Locate and identify every blood parasite.
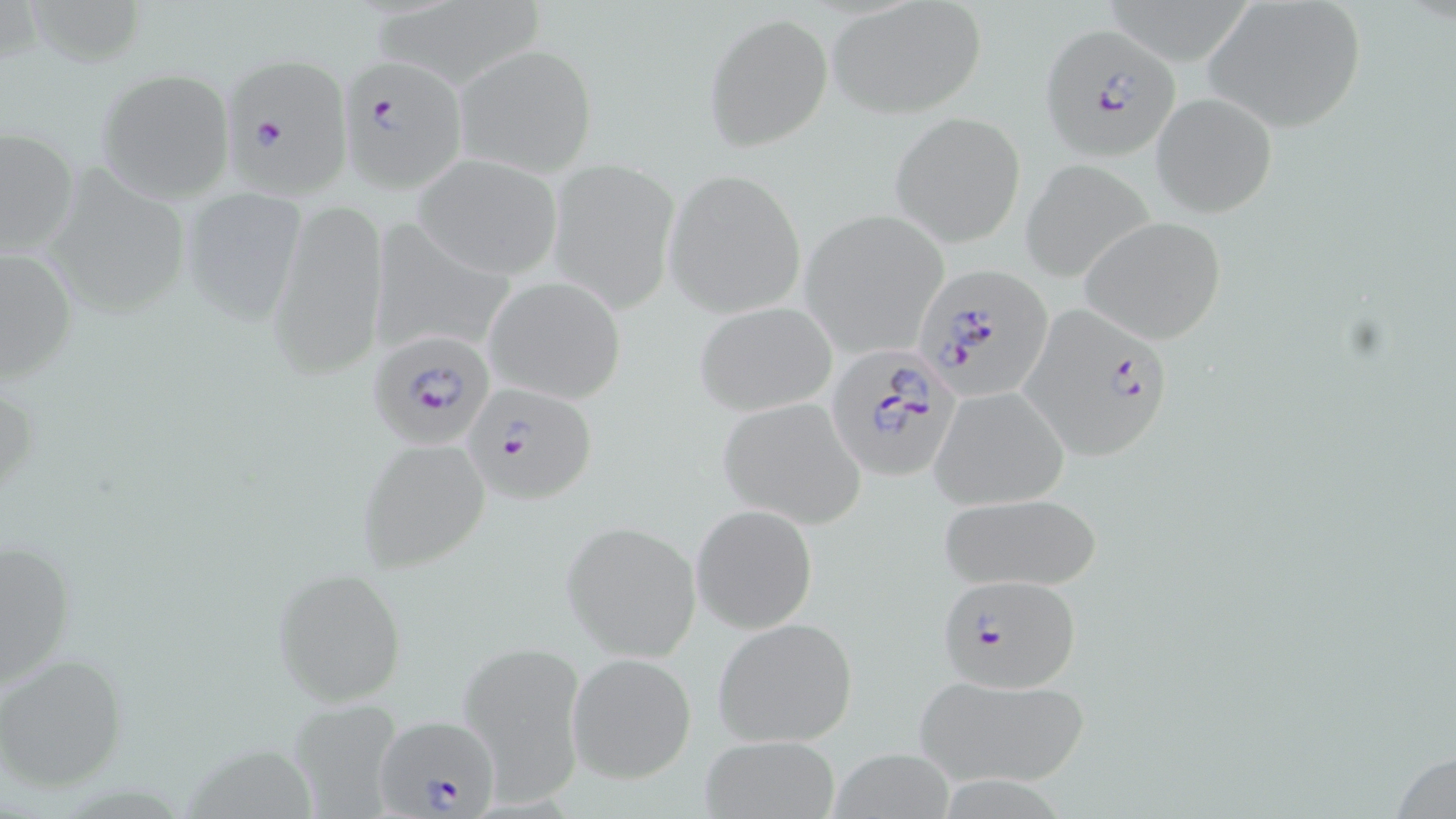
Approximate bounding boxes as [x1, y1, x2, y2] in pixels.
Plasmodium falciparum-infected red blood cells: [1040, 25, 1180, 160], [338, 52, 468, 192], [221, 59, 350, 193], [915, 264, 1052, 396], [1017, 305, 1177, 462], [368, 330, 497, 452], [826, 347, 961, 485], [460, 381, 598, 506], [934, 573, 1084, 693], [377, 713, 504, 819].
No Plasmodium ovale, Plasmodium malariae, Plasmodium vivax, Babesia divergens, or Trypanosoma brucei observed.

Uninfected red blood cell locations: [1204, 0, 1368, 131], [828, 1, 989, 119], [705, 13, 832, 151], [454, 42, 597, 177], [97, 69, 235, 202], [1154, 92, 1277, 218], [889, 110, 1026, 247], [0, 127, 79, 260], [414, 154, 563, 279], [545, 157, 679, 311], [1019, 159, 1155, 282], [39, 165, 194, 321], [664, 169, 809, 318], [180, 184, 309, 324], [266, 197, 390, 380], [799, 211, 949, 358], [1080, 217, 1227, 344], [367, 218, 516, 359], [1, 244, 78, 388], [484, 275, 627, 405], [695, 301, 839, 417], [930, 386, 1069, 508], [717, 398, 865, 529], [358, 437, 489, 571], [938, 491, 1104, 592], [691, 505, 817, 634], [561, 521, 701, 658], [2, 531, 77, 691], [270, 568, 409, 706], [713, 617, 858, 748], [460, 642, 586, 800], [567, 652, 697, 782], [0, 657, 126, 793], [914, 671, 1091, 788], [286, 697, 410, 817], [701, 736, 842, 818]. Slide-level diagnosis: Plasmodium falciparum. Light microscopy. May-Grünwald-Giemsa stain. Image is 1456×819 pixels. Thin blood film. One field of a larger specimen. 1000x magnification.